Give the position of every Plasmodium parasite visible.
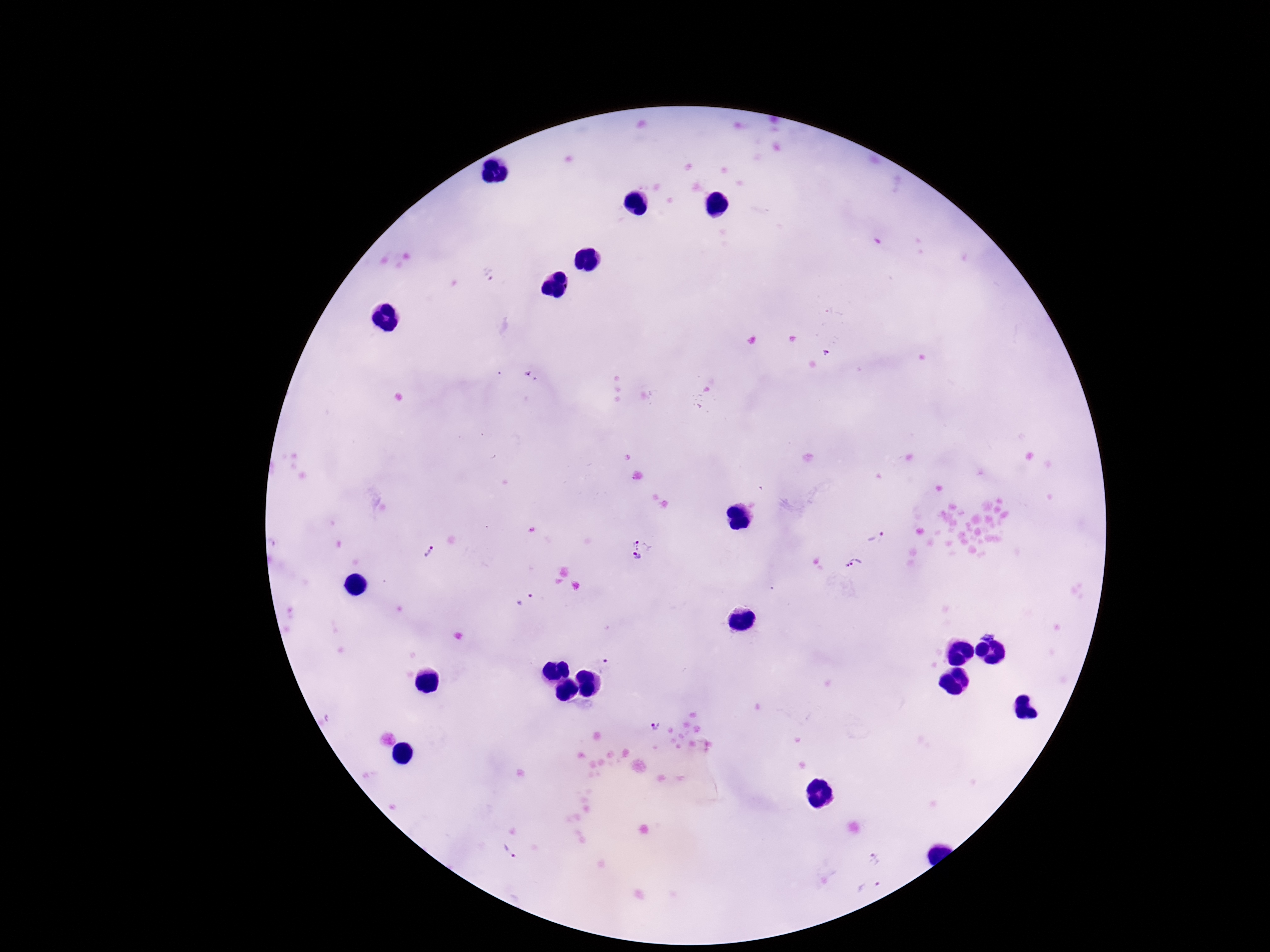
Approximate object centers, in pixels from the top-left corner.
Plasmodium parasites: (x=490, y=277), (x=877, y=536), (x=643, y=545), (x=430, y=551), (x=636, y=558), (x=854, y=565), (x=523, y=599), (x=987, y=632), (x=604, y=665), (x=656, y=724), (x=511, y=854), (x=876, y=858), (x=870, y=889).

Patient malaria status: positive. 100x magnification. Giemsa-stained preparation. Single field of view. Smartphone photograph taken through the microscope eyepiece. Thick peripheral-blood smear. Image is 1270×952 pixels.